Describe the morphology of the erythrocytes.
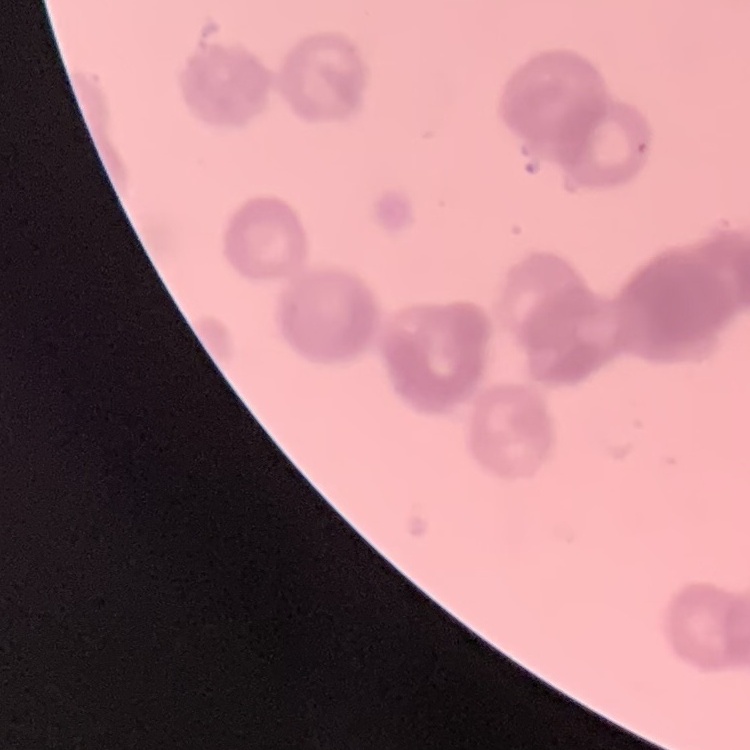

They show rouleaux formation.

stain = Field's or Giemsa
image type = square crop of a larger photomicrograph
preparation = thin blood film